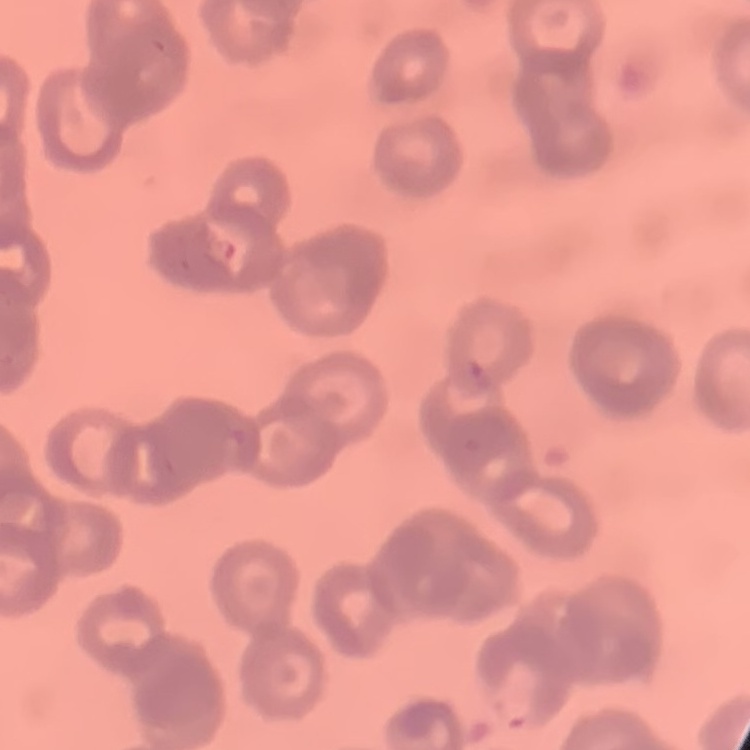
Summary:
  - Erythrocyte morphology: rouleaux formation
  - Preparation: thin blood film
  - Stain: Field's or Giemsa
  - Image type: square crop of a larger photomicrograph